Point out each Plasmodium parasite.
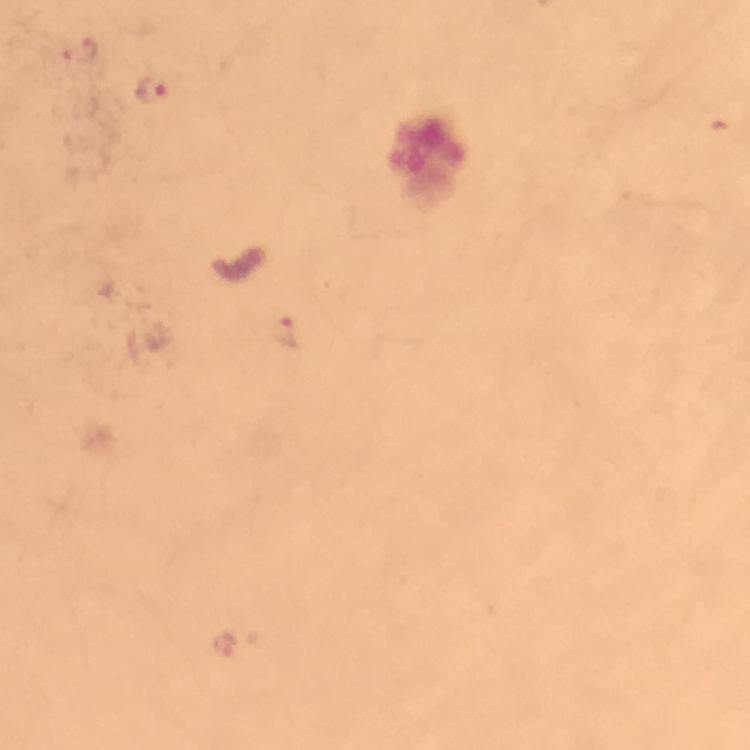

Approximate centers as (x, y) in pixels.
Plasmodium parasites: (78, 51), (151, 89), (281, 334), (224, 644).

capture: smartphone mounted on the microscope
immersion_oil: applied
stain: Giemsa
image_size: 750×750 pixels
cropped_from: a single field of view
preparation: thick smear
magnification: 100x
context: from a malaria diagnostic workup